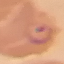 Result: malaria parasites identified. Automatically extracted cell patch, resized to 64 × 64 pixels. Acquired by smartphone through the microscope eyepiece. Giemsa-stained preparation. Thin blood film.